Assess the morphology of the erythrocytes.
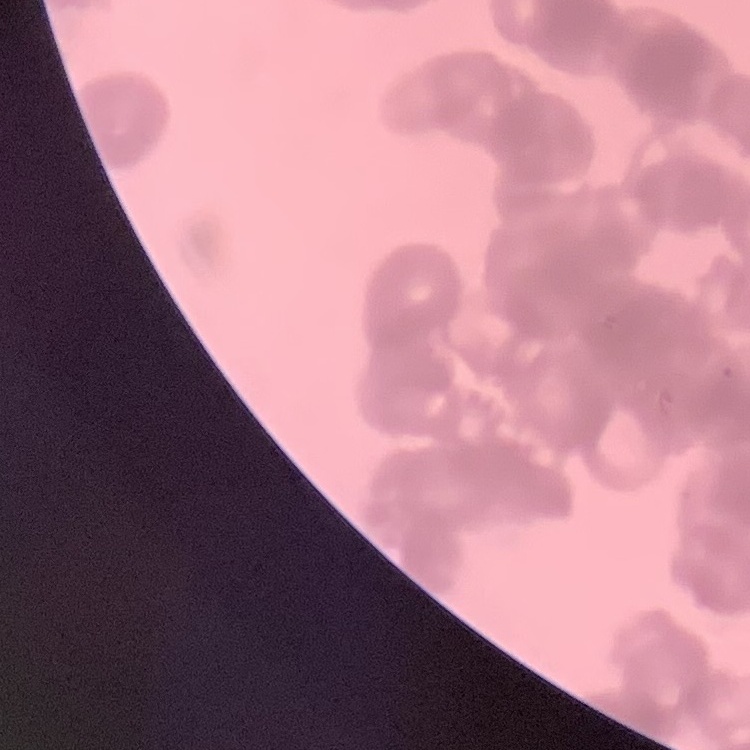
Rouleaux formation.

Thin blood film. Stained with either Field's or Giemsa. One tile cut from a larger photomicrograph.